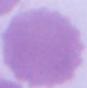

identification: erythrocyte
modality: micrograph
magnification: 1000x